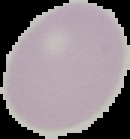

Image is 130×139 pixels. Result: no malaria parasites seen. From a thin blood film. Segmented cell region on a black background.